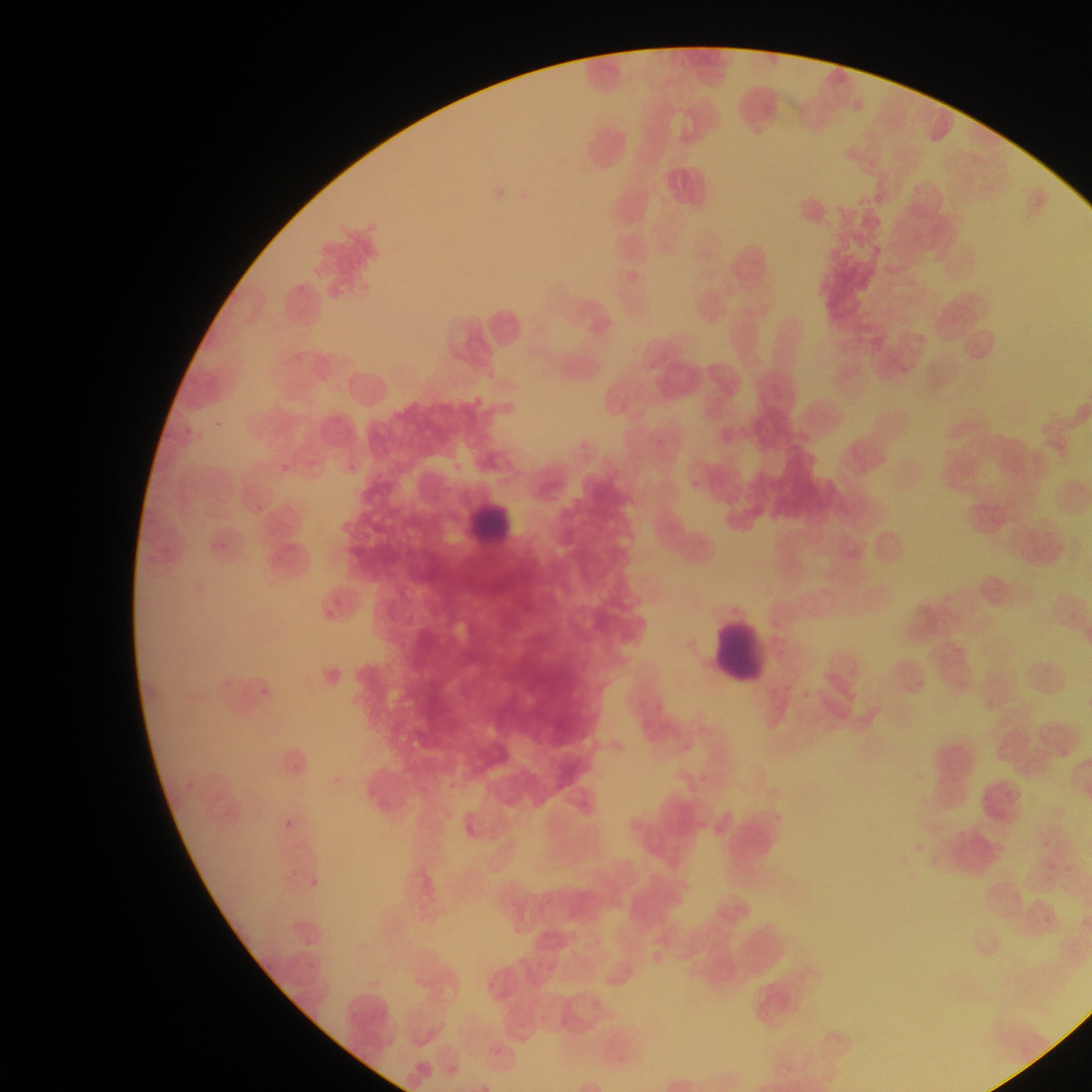
Approximate bounding boxes as (left, top, right, bottom) in pixels.
Summary:
  - Leukocyte locations: (461, 495, 506, 554), (694, 616, 773, 679)
  - Country: Ghana
  - Preparation: thin blood smear
  - Capture: mobile-phone photograph through a microscope
  - Image size: 1092×1092 pixels
  - Field of view: single